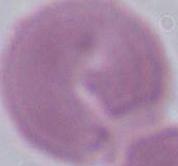

identification = red blood cell
modality = micrograph
magnification = 1000x